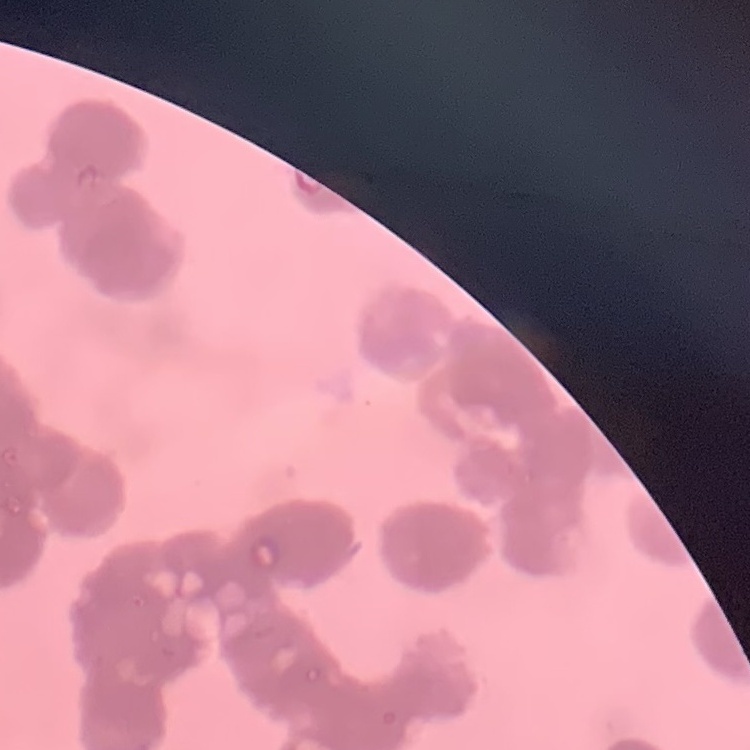

Summary:
  - Erythrocyte morphology: rouleaux formation
  - Preparation: thin peripheral smear
  - Stain: Field's or Giemsa
  - Image type: square crop of a larger photomicrograph